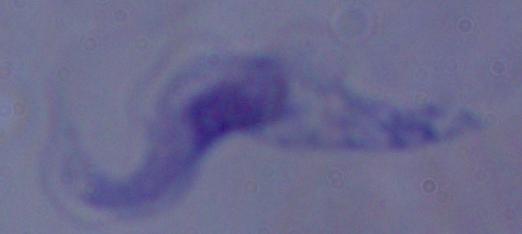 A trypanosome is seen. 1000x magnification. Micrograph.